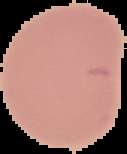
Malaria status: uninfected. Image is 127×154 pixels. Cell region segmented out of the field of view; the surrounding area is masked to black. From a thin blood smear.